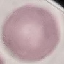

Summary:
  - Result: no malaria parasites seen
  - Preparation: thin blood film
  - Capture: smartphone through the microscope eyepiece
  - Stain: Giemsa
  - Image type: cell patch, automatically extracted from a larger field of view and resized to 64 × 64 pixels